State the blood parasite species.
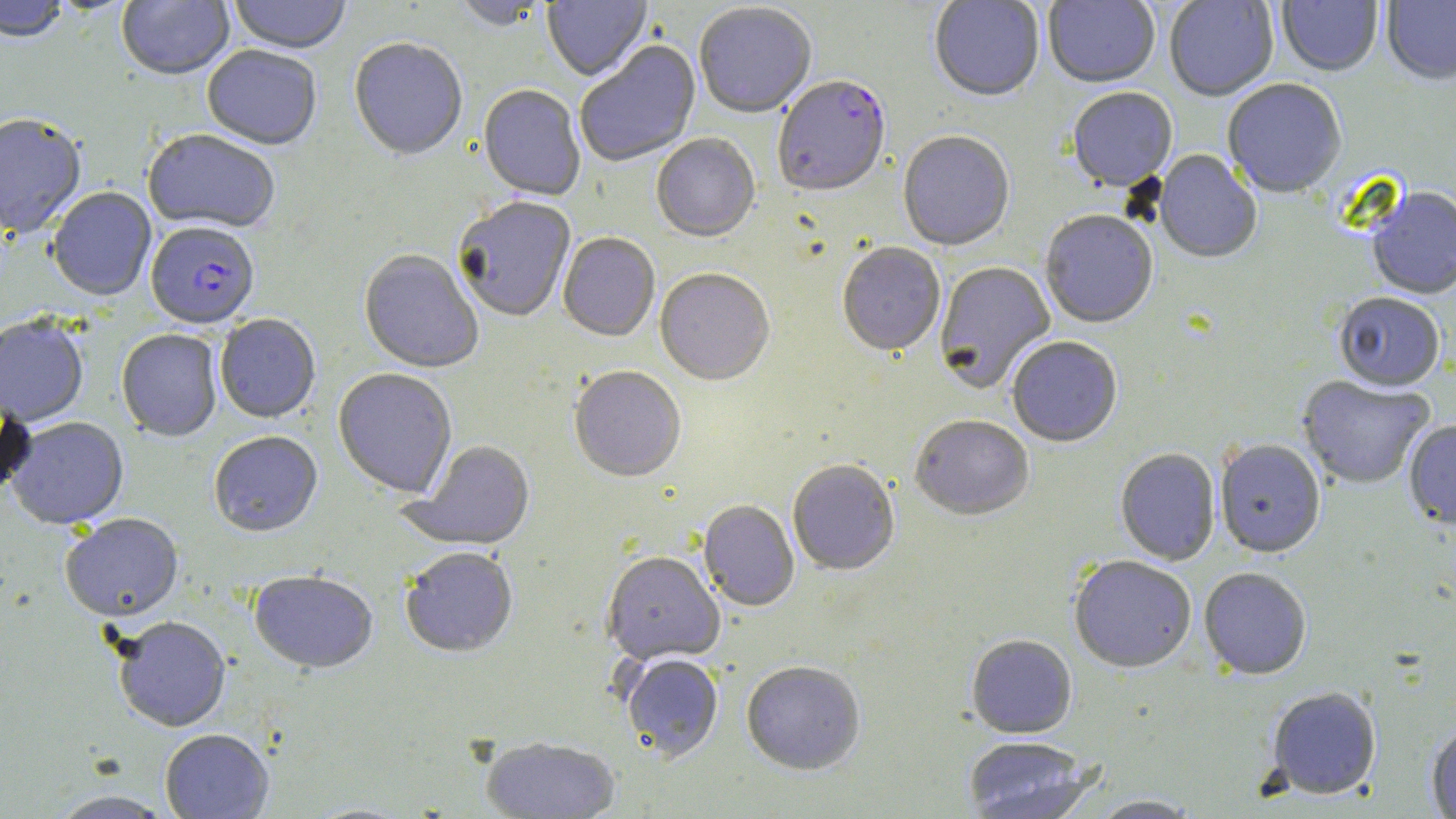

Plasmodium falciparum.

Approximate bounding boxes as [x1, y1, x2, y2] in pixels. Plasmodium falciparum-infected red blood cell locations: [772, 77, 892, 200], [146, 223, 260, 332]. Uninfected red blood cell locations: [0, 0, 68, 45], [228, 0, 352, 57], [542, 0, 652, 83], [929, 0, 1045, 103], [1043, 0, 1160, 90], [1164, 0, 1279, 103], [1277, 0, 1383, 77], [1382, 0, 1456, 87], [117, 1, 234, 82], [452, 1, 550, 31], [694, 4, 817, 120], [349, 39, 468, 163], [575, 42, 702, 169], [202, 47, 321, 152], [1222, 80, 1347, 200], [478, 85, 585, 201], [1067, 89, 1178, 194], [0, 115, 86, 242], [142, 131, 280, 235], [897, 132, 1015, 253], [651, 135, 760, 244], [1153, 150, 1262, 265], [1366, 187, 1456, 301], [47, 188, 157, 303], [453, 198, 576, 324], [1040, 211, 1158, 331], [558, 234, 660, 343], [837, 244, 946, 359], [358, 250, 484, 375], [935, 262, 1055, 393], [655, 270, 775, 388], [1333, 294, 1444, 393], [215, 315, 321, 424], [0, 317, 89, 428], [117, 330, 222, 443], [1007, 338, 1122, 449], [569, 368, 686, 485], [333, 369, 457, 499], [1297, 376, 1434, 490], [910, 417, 1033, 523], [7, 419, 129, 531], [1403, 421, 1456, 532], [208, 433, 323, 539], [402, 441, 537, 552], [1214, 441, 1326, 560], [1115, 449, 1220, 566], [787, 461, 900, 577], [698, 501, 799, 612], [60, 516, 184, 624], [401, 549, 518, 660], [602, 554, 724, 667], [1069, 557, 1196, 676], [1199, 569, 1312, 681], [249, 573, 377, 677], [113, 619, 231, 734], [966, 637, 1077, 740], [620, 655, 723, 764], [741, 664, 865, 777], [1266, 689, 1382, 800], [1426, 724, 1456, 819], [160, 731, 274, 819], [962, 738, 1097, 819], [480, 739, 620, 818], [51, 791, 171, 819], [1087, 796, 1202, 818]. Captured at 1000x magnification. Thin blood film. Image is 1456×819 pixels. May-Grünwald-Giemsa-stained preparation. One field of a larger specimen. Optical microscopy.